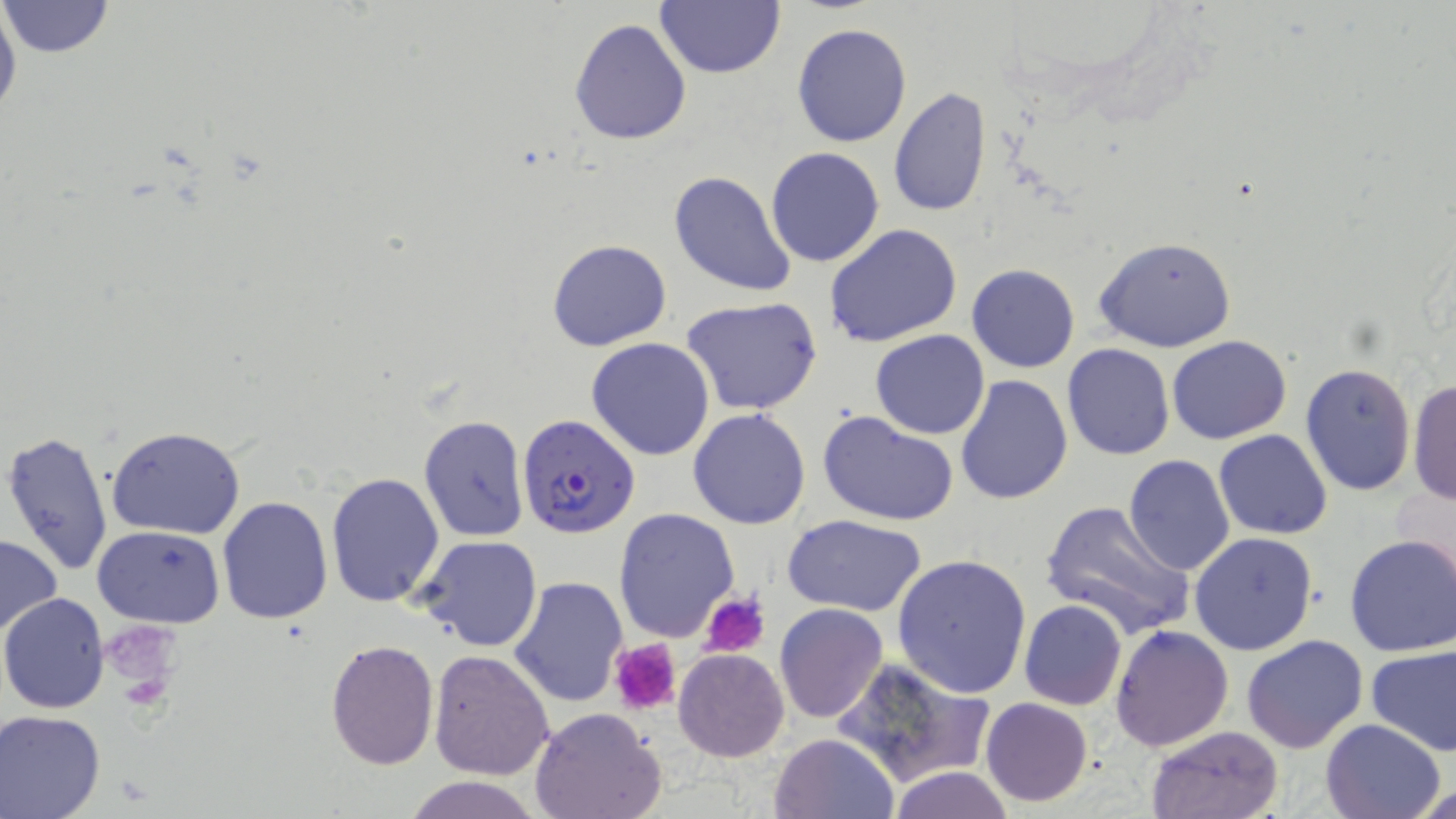

slide_level_diagnosis: Plasmodium falciparum
stain: May-Grünwald-Giemsa
magnification: 1000x
modality: light microscopy
uninfected_red_blood_cell_locations: 'approximate bounding boxes as (x1, y1, x2, y2) in pixels: (0, 0, 21, 133), (655, 0, 784, 79), (1, 1, 114, 58), (569, 18, 693, 145), (792, 23, 912, 147), (887, 88, 990, 216), (766, 147, 885, 267), (669, 170, 799, 297), (825, 223, 964, 350), (1093, 236, 1238, 353), (547, 238, 671, 352), (967, 263, 1078, 372), (681, 297, 824, 418), (870, 330, 991, 439), (1167, 335, 1292, 444), (586, 337, 714, 461), (1062, 342, 1175, 460), (1299, 363, 1416, 498), (953, 373, 1073, 504), (1407, 377, 1456, 505), (688, 408, 813, 529), (819, 411, 958, 527), (417, 412, 531, 542), (104, 426, 246, 539), (2, 430, 114, 579), (1213, 430, 1333, 540), (1122, 456, 1234, 576), (324, 471, 446, 608), (216, 495, 335, 624), (1039, 500, 1195, 639), (612, 508, 740, 640), (785, 514, 928, 615), (93, 525, 223, 627), (1190, 531, 1319, 655), (1344, 533, 1456, 657), (0, 534, 62, 639), (414, 534, 543, 651), (891, 554, 1032, 698), (509, 576, 628, 708), (1, 593, 112, 712), (1018, 600, 1127, 711), (775, 603, 888, 723), (1110, 626, 1233, 751), (1241, 635, 1368, 755), (326, 639, 439, 768), (1365, 645, 1456, 756), (674, 647, 789, 761), (427, 649, 555, 779), (835, 657, 992, 788), (980, 697, 1094, 806), (530, 705, 668, 819), (1, 710, 106, 819), (1321, 718, 1446, 819), (1145, 726, 1284, 819), (769, 732, 899, 818), (889, 767, 1015, 819), (401, 775, 547, 819), (1414, 781, 1455, 819)'
plasmodium_falciparum_infected_red_blood_cell_locations: 'approximate bounding boxes as (x1, y1, x2, y2) in pixels: (516, 412, 639, 540)'
field_of_view: single
image_size: 1456×819 pixels
preparation: thin blood smear
platelet_locations: 'approximate bounding boxes as (x1, y1, x2, y2) in pixels: (702, 593, 770, 657), (102, 626, 184, 680), (611, 639, 682, 715)'